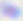
Summary:
  - Modality: micrograph
  - Magnification: 400x
  - Identification: Toxoplasma gondii